State which cell type is depicted.
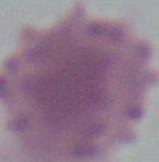

An erythrocyte.

Summary:
  - Modality: photomicrograph
  - Magnification: 1000x